Assess the morphology of the erythrocytes.
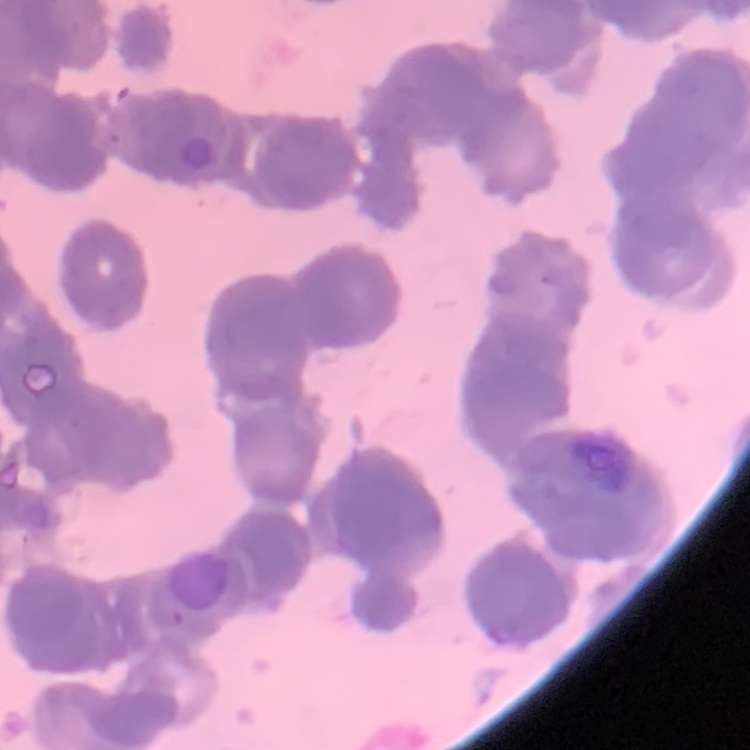
Rouleaux formation.

Summary:
  - Preparation: thin blood smear
  - Stain: Field's or Giemsa
  - Image type: square crop of a larger photomicrograph